Point out each malaria parasite and each leukocyte.
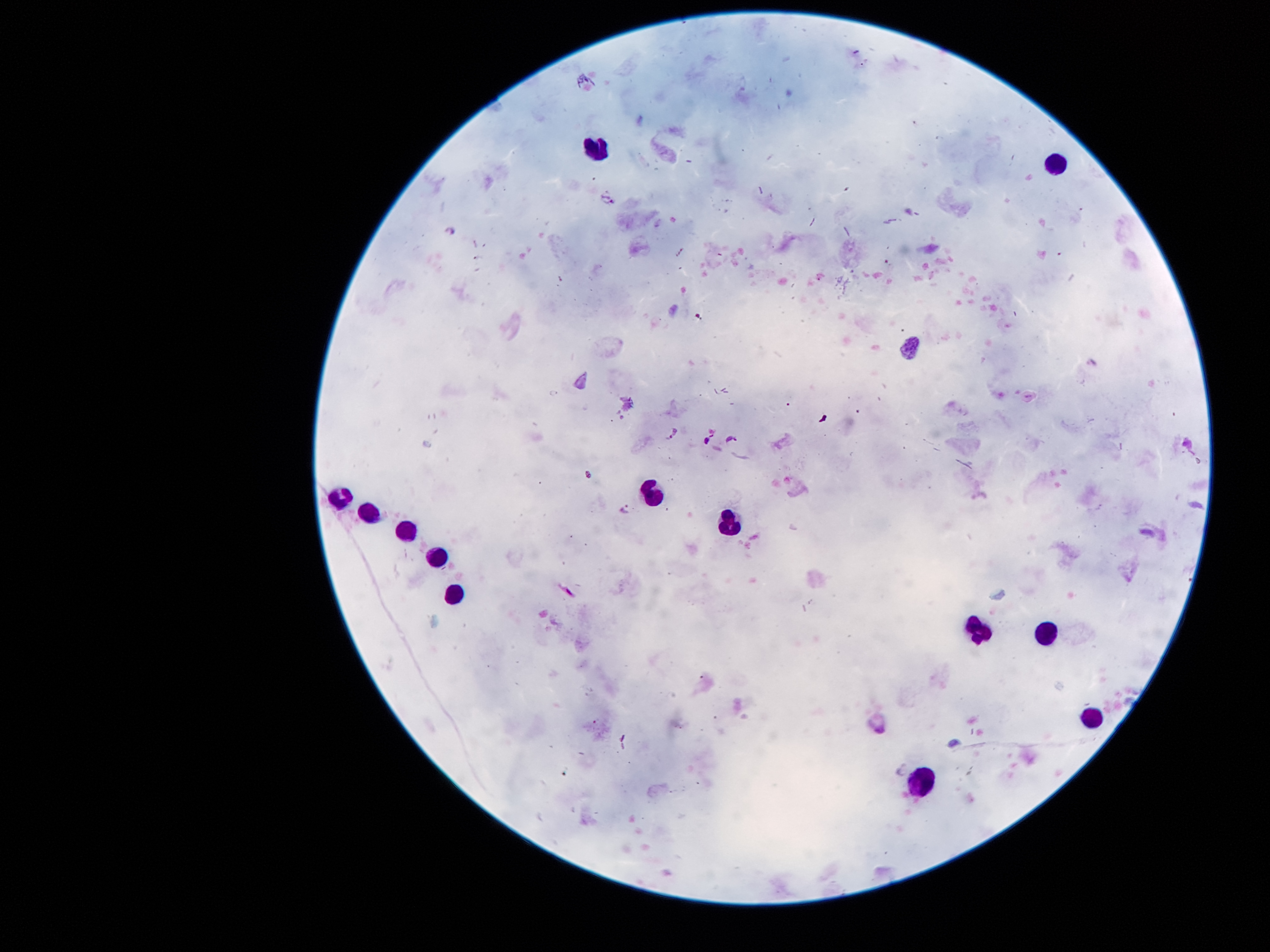

Approximate centers as [x, y] in pixels.
Malaria parasites: [606, 200], [671, 435], [732, 439], [626, 509].
Leukocytes: [595, 148], [1053, 162], [651, 494], [343, 497], [368, 512], [726, 519], [406, 529], [437, 556], [452, 590], [975, 628], [1044, 635], [1093, 715], [919, 781].

Single field of view. Patient malaria status: positive for Plasmodium falciparum. Image is 1270×952 pixels. Giemsa-stained preparation. Smartphone photograph taken through the microscope eyepiece. 100x magnification. Thick blood film.